Point out each Plasmodium parasite.
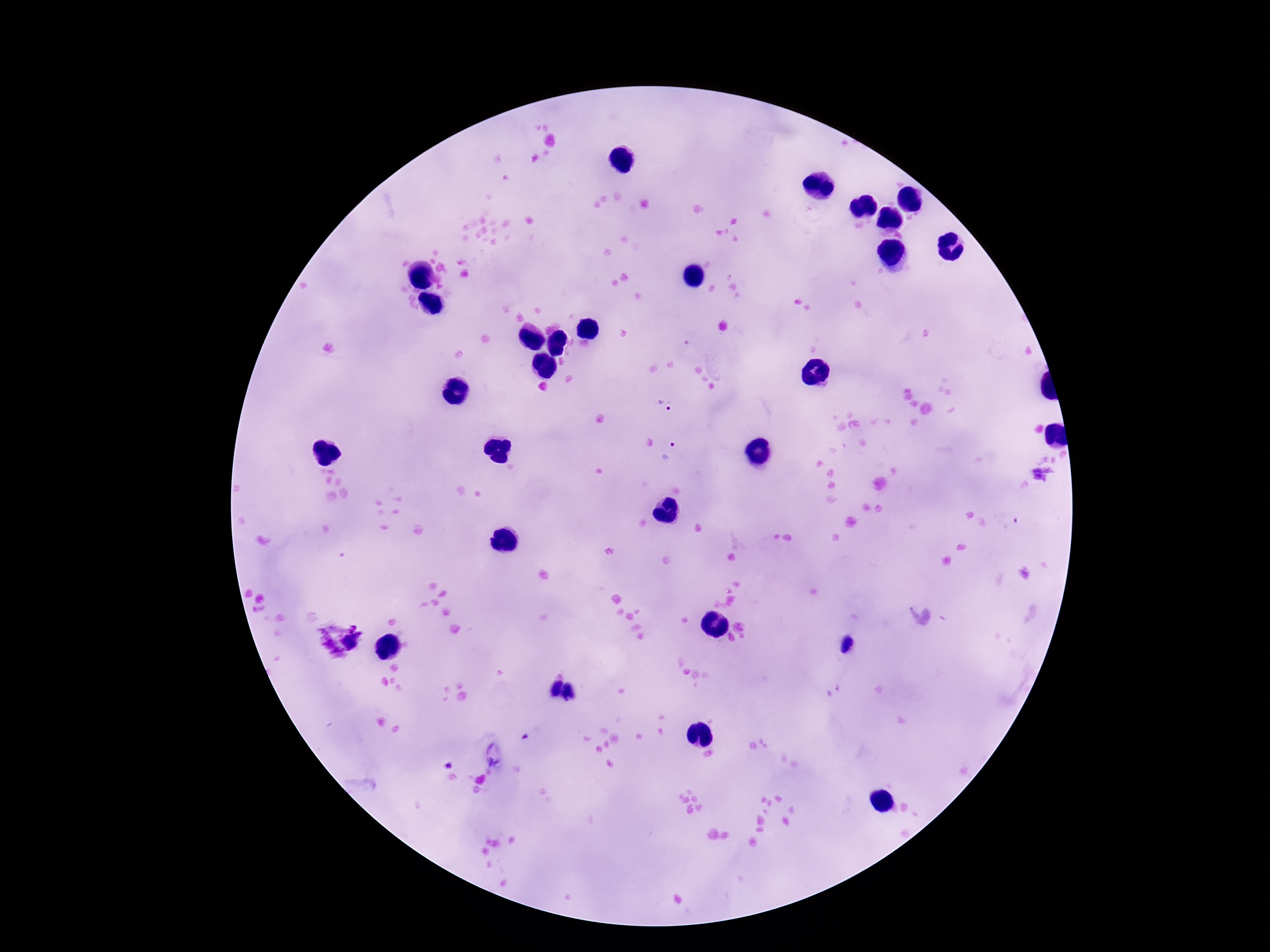
Approximate centers as [x, y] in pixels.
Plasmodium parasites: [664, 405], [672, 453], [1044, 476], [351, 642].

preparation = thick peripheral-blood smear
patient malaria status = positive
magnification = 100x
field of view = one from this slide
capture = smartphone camera through the microscope eyepiece
stain = Giemsa
image size = 1270×952 pixels